Assess this cell for malaria.
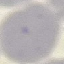

Uninfected.

{
  "preparation": "thin blood film",
  "stain": "Giemsa",
  "capture": "smartphone camera at the microscope eyepiece",
  "image_type": "cell patch, automatically extracted from a larger field of view and resized to 64 × 64 pixels"
}